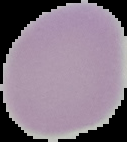
Summary:
  - Image type: segmented cell region with the area outside set to black
  - Preparation: thin blood smear
  - Image size: 127×142 pixels
  - Result: no malaria parasites detected